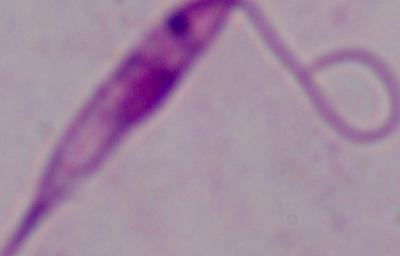
Summary:
  - Magnification: 1000x
  - Identification: Leishmania
  - Modality: photomicrograph